Report the malaria status of this cell.
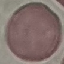

It is uninfected.

capture = smartphone through the microscope eyepiece
image type = automatically extracted cell patch, resized to 64 × 64 pixels
preparation = thin blood smear
stain = Giemsa